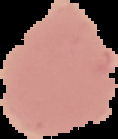

From a thin blood smear. Result: negative for malaria parasites. Image is 118×139 pixels. Cell region segmented out of the field of view; the surrounding area is masked to black.